Identify the blood parasite species.
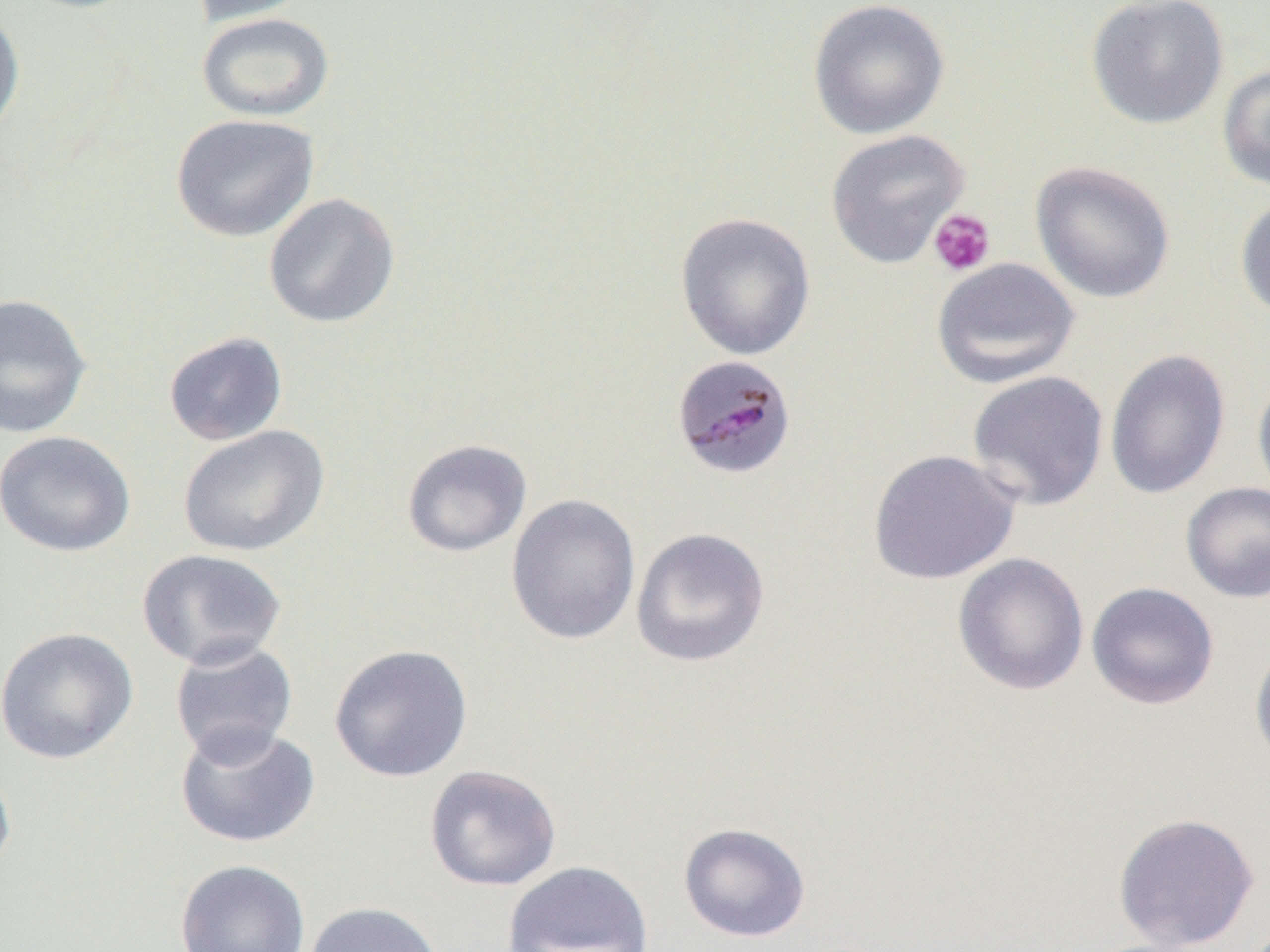
Plasmodium malariae.

Summary:
  - Coordinate format: approximate bounding boxes as (x1,y1)-(x2,y2) corner pairs in pixels
  - Plasmodium malariae-infected red blood cell locations: (670,354)-(797,480)
  - Uninfected red blood cell locations: (189,0)-(312,26), (807,0)-(951,140), (1086,0)-(1229,129), (0,6)-(25,142), (196,11)-(335,122), (1217,64)-(1270,194), (170,113)-(318,242), (825,129)-(970,268), (1030,160)-(1175,303), (263,193)-(401,329), (1235,195)-(1270,322), (675,212)-(816,361), (930,257)-(1080,389), (0,293)-(92,439), (163,331)-(288,446), (1104,349)-(1232,500), (967,370)-(1109,510), (1252,371)-(1270,505), (177,425)-(329,557), (1,430)-(136,557), (401,438)-(532,557), (867,449)-(1021,585), (1180,482)-(1270,603), (505,492)-(641,645), (631,527)-(770,668), (137,548)-(288,670), (952,552)-(1089,696), (1086,581)-(1220,710), (0,626)-(138,764), (168,638)-(298,763), (1249,640)-(1270,770), (329,644)-(474,783), (174,722)-(320,849), (0,759)-(17,883), (424,764)-(562,891), (1112,812)-(1261,951), (677,822)-(812,942), (174,859)-(310,952), (501,860)-(654,952), (302,901)-(444,952)
  - Platelet locations: (927,210)-(996,277)
  - Modality: optical microscopy
  - Preparation: thin blood smear
  - Field of view: one of a larger specimen
  - Image size: 1270×952 pixels
  - Magnification: 1000x